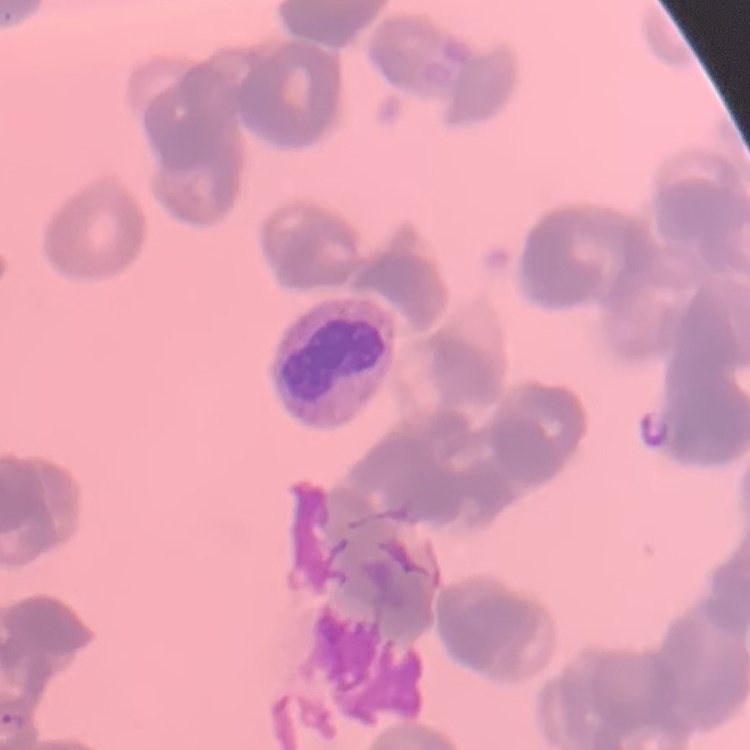

Summary:
  - Erythrocyte morphology: rouleaux formation
  - Preparation: thin peripheral smear
  - Image type: square crop of a larger photomicrograph
  - Stain: Field's or Giemsa